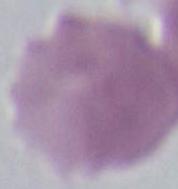

{
  "modality": "micrograph",
  "identification": "red blood cell",
  "magnification": "1000x"
}